Point out every Plasmodium parasite.
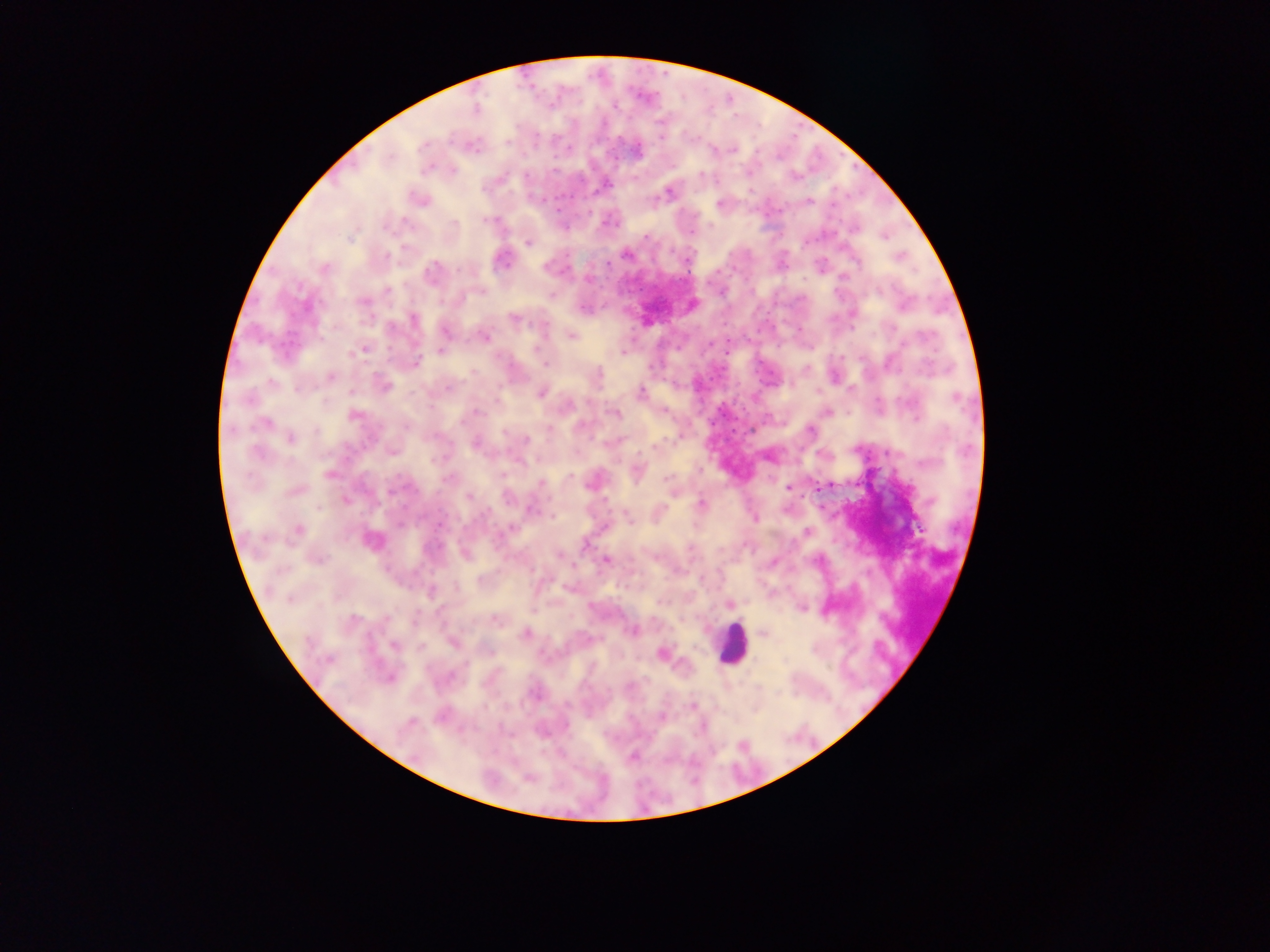
Approximate centers as [x, y] in pixels.
Plasmodium parasites: [476, 108], [467, 146], [569, 149], [636, 150], [732, 150], [713, 151], [427, 165], [554, 172], [699, 173], [704, 173], [584, 174], [529, 175], [717, 179], [604, 185], [667, 193], [653, 197], [807, 201], [717, 202], [558, 208], [888, 235], [645, 237], [528, 242], [625, 255], [499, 258], [856, 262], [546, 266], [432, 270], [466, 270], [588, 279], [878, 291], [855, 311], [768, 314], [413, 319], [514, 320], [723, 325], [761, 328], [572, 336], [485, 337], [727, 341], [710, 344], [778, 345], [441, 350], [622, 350], [725, 352], [350, 353], [417, 361], [805, 367], [330, 375], [597, 377], [712, 378], [383, 384], [446, 386], [640, 391], [542, 392], [876, 398], [717, 409], [476, 412], [614, 412], [352, 416], [268, 421], [548, 430], [502, 431], [809, 431], [290, 438], [526, 439], [476, 441], [392, 449], [817, 453], [329, 473], [446, 479], [668, 481], [542, 482], [788, 487], [828, 487], [294, 491], [468, 495], [347, 500], [702, 503], [659, 512], [754, 517], [629, 519], [296, 529], [805, 532], [370, 541], [585, 543], [690, 551], [465, 554], [558, 555], [817, 558], [607, 561], [538, 581], [454, 589], [431, 593], [662, 600], [729, 602], [804, 609], [351, 616], [494, 621], [633, 630], [525, 633], [764, 635], [453, 643], [394, 645], [420, 647], [662, 654], [542, 656], [389, 677], [628, 685], [631, 688], [536, 692], [690, 703], [485, 707], [440, 716], [505, 731], [508, 733], [632, 756].

Summary:
  - Field of view: single
  - Capture: mobile-phone photograph through a microscope
  - Preparation: thick blood smear
  - Image size: 1270×952 pixels
  - Country: Ghana